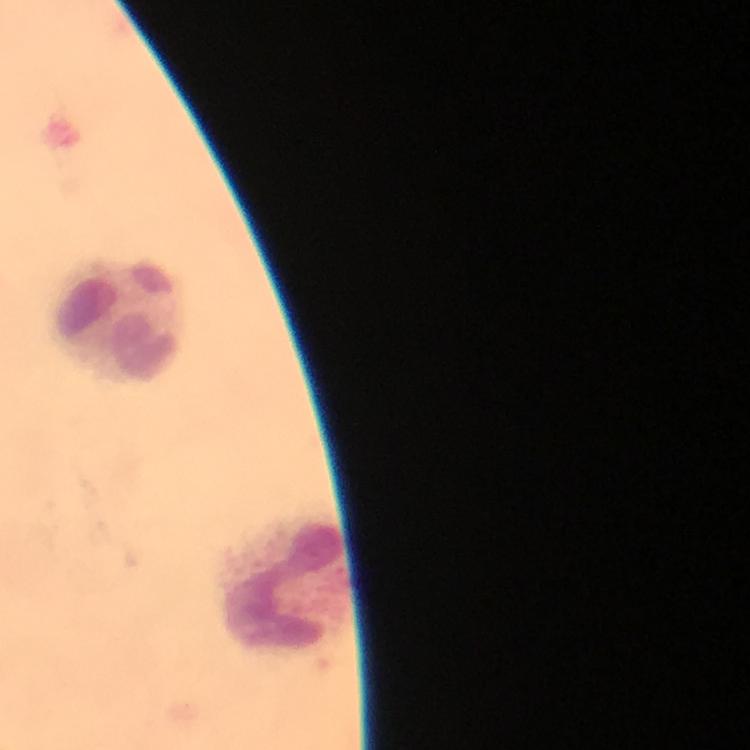

Approximate centers as [x, y] in pixels. Leukocyte locations: [118, 320], [285, 579]. Image is 750×750 pixels. At 100x magnification. Immersion oil applied. Thick smear. From a diagnostic examination for malaria. Giemsa-stained preparation. A crop from one field of view. Plasmodium parasites: none detected. Photographed with a smartphone mounted on the microscope.